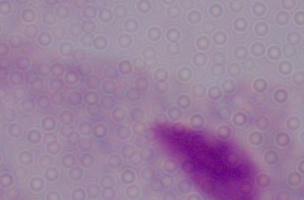
A trichomonad is seen. Micrograph. 1000x magnification.